Give the position of every malaria parasite.
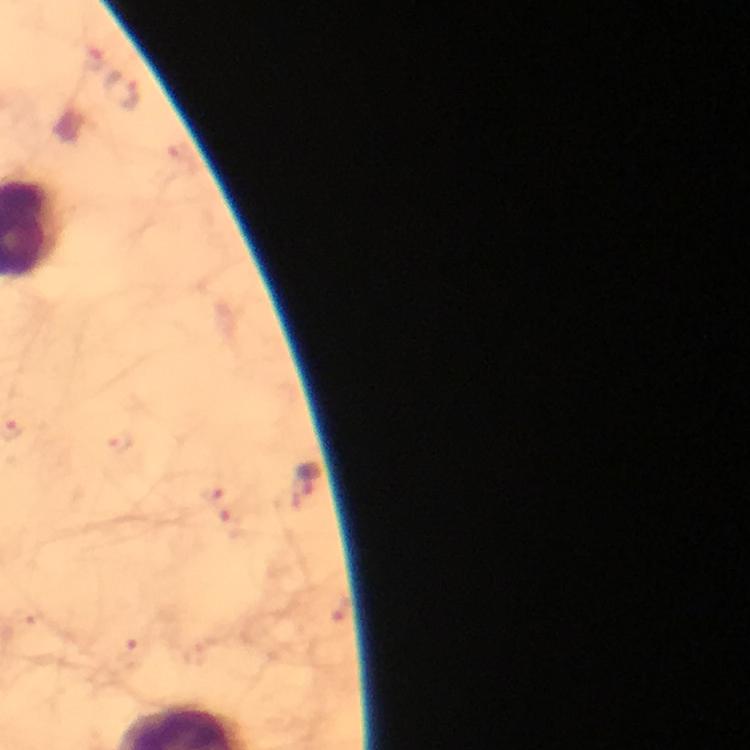
Approximate object centers, in pixels from the top-left corner.
Malaria parasites: (x=121, y=93), (x=308, y=478).

100x magnification. Image is 750×750 pixels. From a diagnostic examination for malaria. Photographed through the microscope with a smartphone camera. Immersion oil applied. Giemsa stain. Cropped region of a single field of view. Thick blood smear.